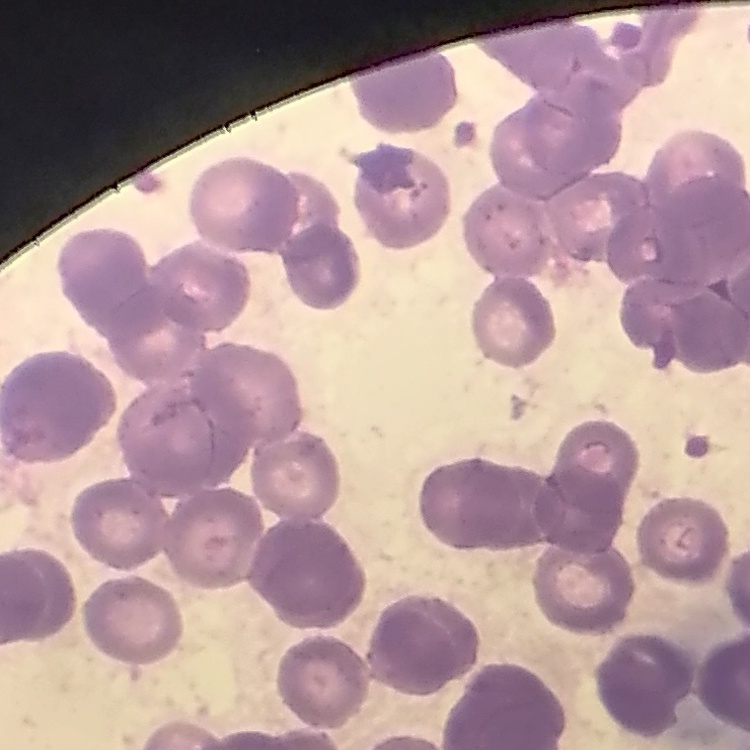
Summary:
  - Red blood cell morphology: rouleaux formation
  - Image type: one tile cut from a larger photomicrograph
  - Stain: Field's or Giemsa
  - Preparation: thin blood smear